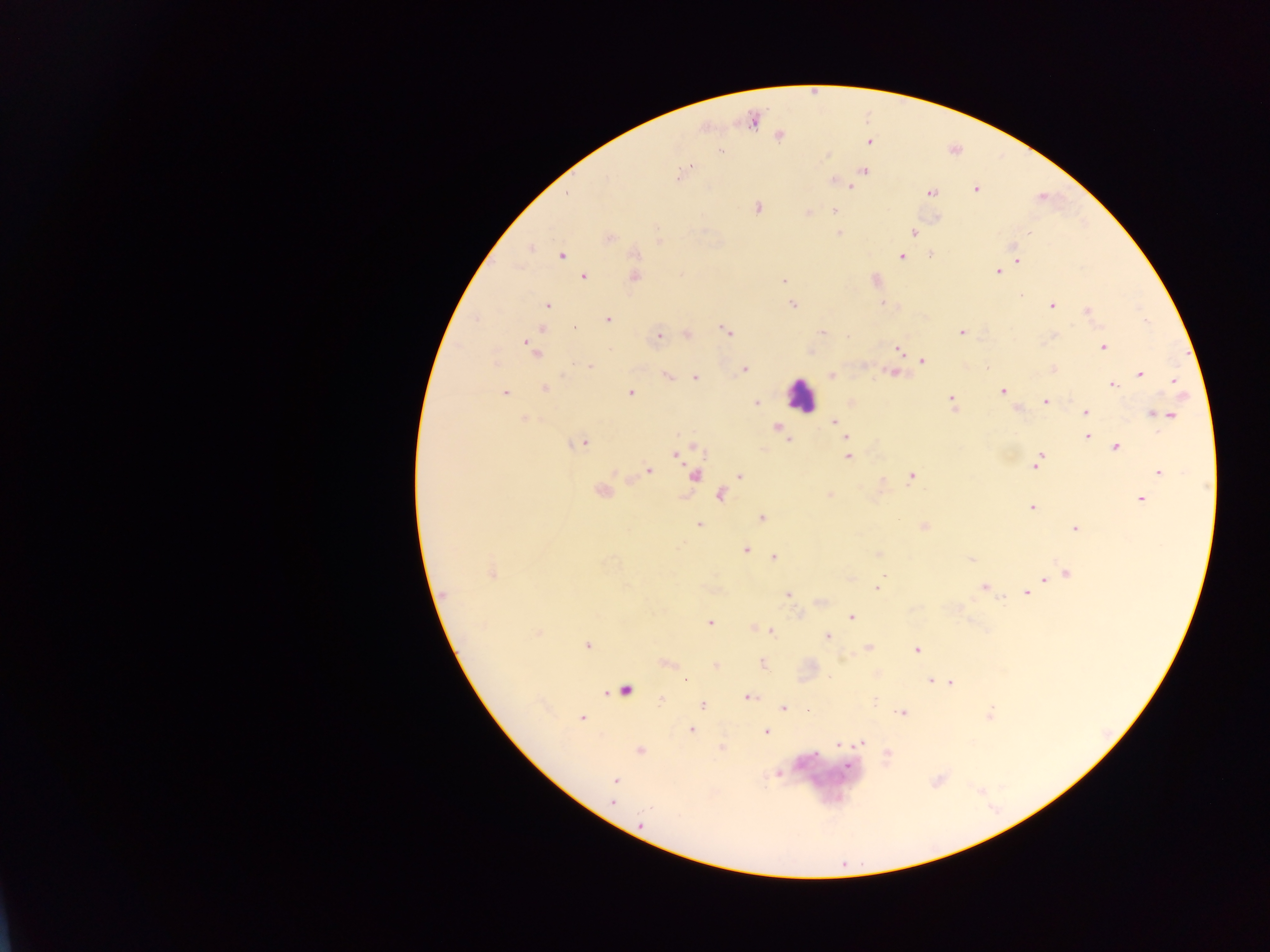

{
  "capture": "mobile-phone photograph through a microscope",
  "image_size": "1270×952 pixels",
  "plasmodium_parasite_locations": "approximate centers as x y in pixels: 779 138; 868 143; 721 152; 825 156; 691 164; 693 166; 864 170; 859 172; 830 180; 851 186; 931 193; 757 207; 835 209; 807 212; 838 232; 912 232; 610 238; 1027 238; 530 249; 931 255; 561 256; 901 257; 1018 260; 996 273; 583 276; 635 277; 783 280; 791 304; 547 306; 1052 306; 1086 310; 607 321; 542 328; 719 329; 725 330; 962 330; 821 331; 538 333; 686 333; 657 334; 728 334; 848 335; 1103 346; 530 347; 897 349; 924 359; 590 367; 744 370; 888 372; 666 374; 1138 374; 832 376; 695 377; 1174 378; 1114 385; 545 390; 629 390; 503 391; 1003 391; 756 402; 951 402; 1044 402; 1015 410; 1085 412; 1155 415; 1171 415; 524 418; 834 421; 777 427; 1087 436; 845 438; 580 442; 1116 448; 1043 454; 674 456; 848 456; 1038 458; 1035 466; 648 471; 1158 471; 694 475; 910 475; 740 476; 600 491; 719 495; 830 495; 1138 498; 1032 508; 762 518; 758 520; 699 524; 925 527; 1073 529; 745 548; 749 551; 879 553; 774 559; 971 560; 491 573; 1067 573; 1044 579; 982 585; 877 588; 442 593; 787 593; 1025 593; 1003 600; 819 601; 797 613; 852 616; 709 624; 754 628; 771 631; 829 637; 587 645; 866 648; 915 650; 840 660; 762 664; 716 666; 929 678; 685 680; 945 681; 951 683; 626 691; 748 696; 661 699; 702 705; 781 708; 806 710; 901 711; 582 718; 693 729; 767 733; 860 743; 835 744; 721 747; 641 751; 777 775; 615 781; 612 804",
  "country": "Ghana",
  "preparation": "thick blood smear",
  "leukocyte_locations": "approximate centers as x y in pixels: 797 391",
  "field_of_view": "single"
}